Locate platelets.
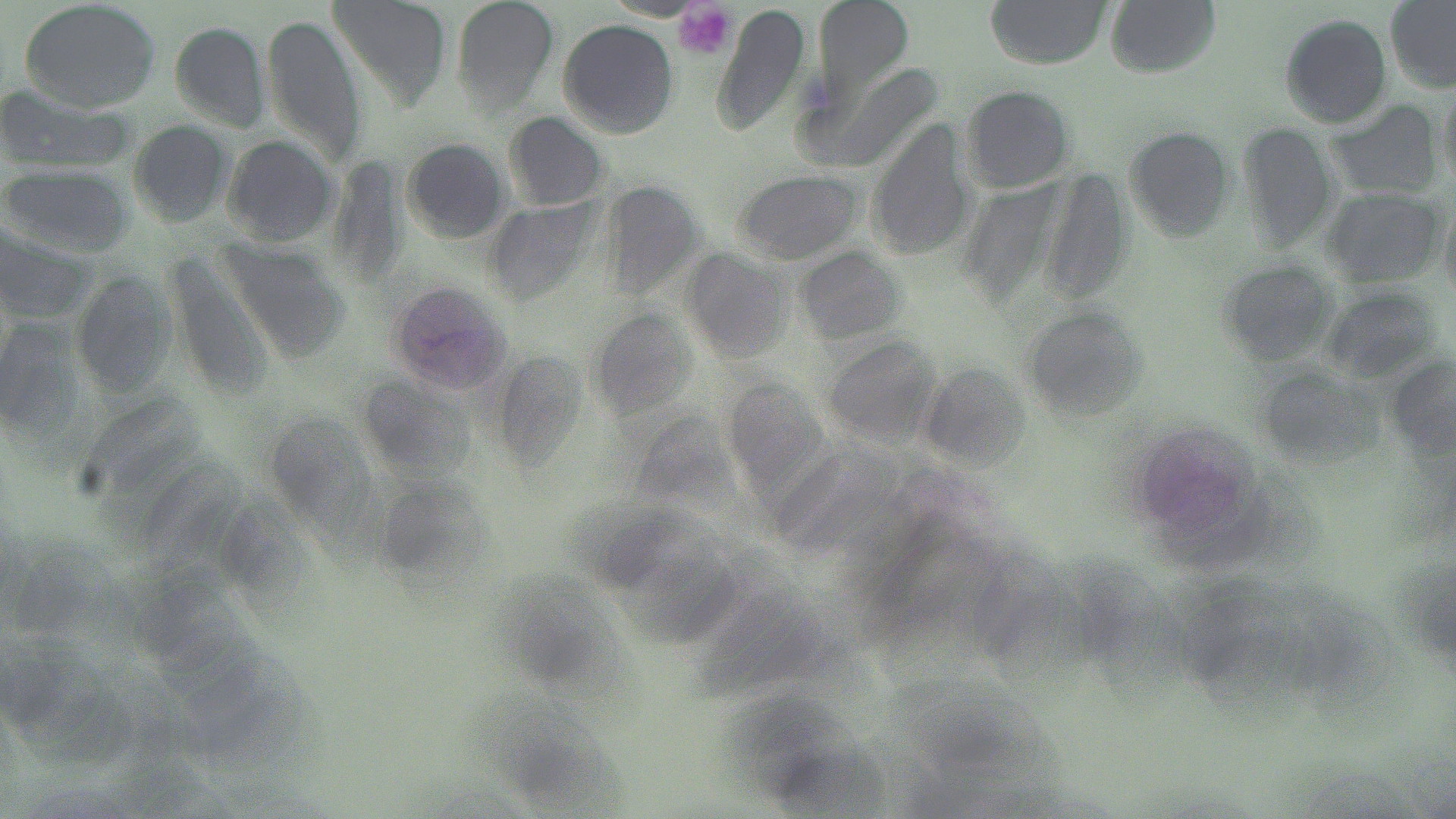
Approximate bounding boxes as named x1/y1/x2/y2 corners in pixels.
Platelets: (x1=676, y1=1, x2=736, y2=59).

Uninfected red blood cell locations: (x1=17, y1=0, x2=163, y2=114), (x1=450, y1=0, x2=559, y2=112), (x1=817, y1=0, x2=913, y2=104), (x1=984, y1=0, x2=1111, y2=68), (x1=1107, y1=0, x2=1222, y2=75), (x1=1384, y1=0, x2=1456, y2=87), (x1=328, y1=1, x2=449, y2=109), (x1=1277, y1=15, x2=1394, y2=129), (x1=261, y1=16, x2=368, y2=160), (x1=164, y1=18, x2=270, y2=128), (x1=556, y1=21, x2=679, y2=137), (x1=960, y1=85, x2=1077, y2=194), (x1=0, y1=87, x2=135, y2=175), (x1=1324, y1=98, x2=1446, y2=205), (x1=505, y1=111, x2=610, y2=210), (x1=126, y1=121, x2=238, y2=226), (x1=1122, y1=121, x2=1233, y2=240), (x1=1233, y1=122, x2=1338, y2=247), (x1=867, y1=123, x2=974, y2=262), (x1=222, y1=134, x2=339, y2=246), (x1=399, y1=138, x2=512, y2=246), (x1=2, y1=164, x2=134, y2=257), (x1=732, y1=167, x2=861, y2=268), (x1=1321, y1=188, x2=1445, y2=287), (x1=0, y1=225, x2=92, y2=328), (x1=223, y1=236, x2=348, y2=359), (x1=794, y1=243, x2=904, y2=344), (x1=679, y1=245, x2=793, y2=363), (x1=1218, y1=262, x2=1340, y2=365), (x1=69, y1=273, x2=178, y2=393), (x1=385, y1=281, x2=513, y2=398), (x1=1017, y1=308, x2=1146, y2=427), (x1=1, y1=324, x2=79, y2=437), (x1=825, y1=337, x2=942, y2=446), (x1=1389, y1=356, x2=1454, y2=460). Slide-level diagnosis: Plasmodium vivax. May-Grünwald-Giemsa-stained preparation. 1000x magnification. Thin blood smear. Light microscopy. One field of a larger specimen. Image is 1456×819 pixels.